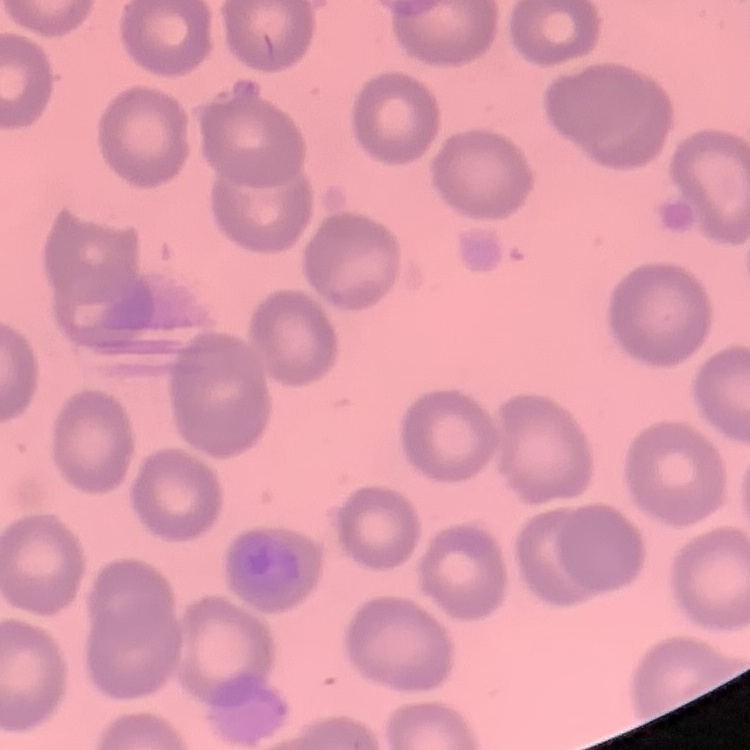

red blood cell morphology = no rouleaux formation
preparation = thin blood film
image type = square crop of a larger photomicrograph
stain = Field's or Giemsa